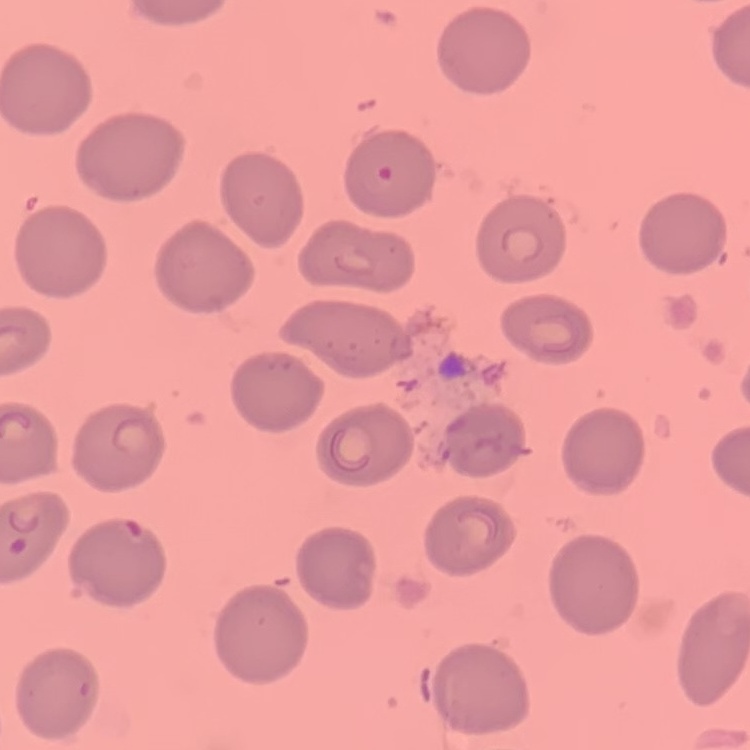
Summary:
  - Red blood cell morphology: no rouleaux formation
  - Stain: Field's or Giemsa
  - Image type: square crop of a larger photomicrograph
  - Preparation: thin peripheral smear